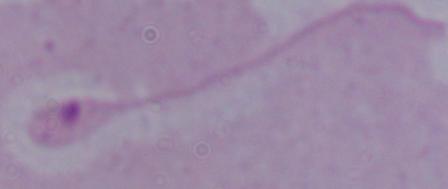
Summary:
  - Identification: Leishmania
  - Modality: micrograph
  - Magnification: 1000x